Comment on the morphology of the red blood cells.
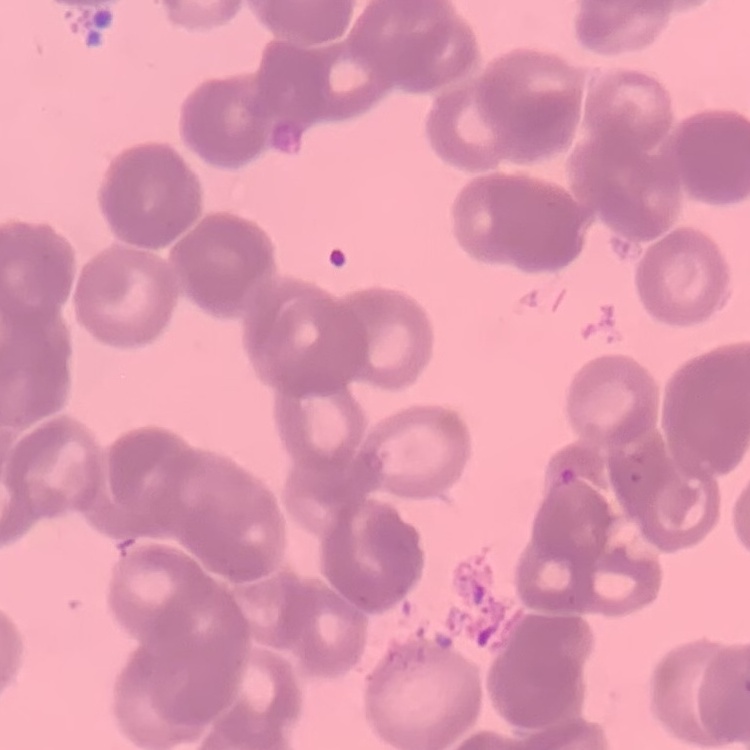

Rouleaux formation.

Stained with either Field's or Giemsa. Thin blood smear. Square crop of a larger photomicrograph.